Assess this cell for malaria.
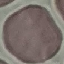
It is uninfected.

Thin blood smear. Cell patch, automatically extracted from a larger field of view and resized to 64 × 64 pixels. Acquired by smartphone through the microscope eyepiece. Giemsa stain.